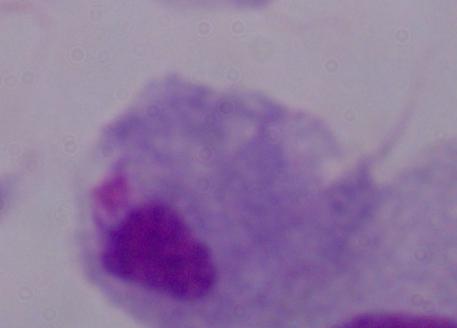
identification = trichomonad
modality = micrograph
magnification = 1000x